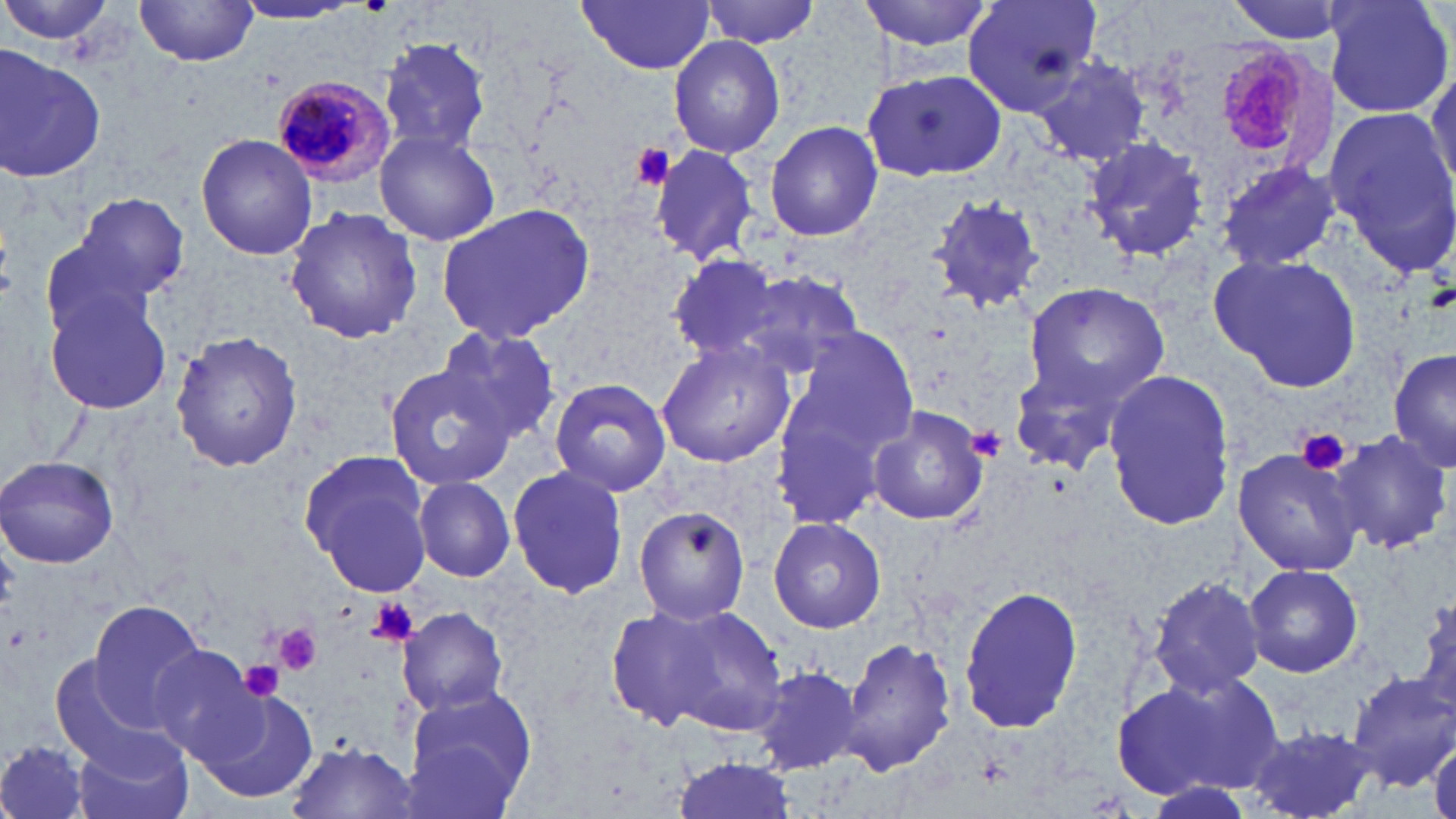

Approximate bounding boxes as named x1/y1/x2/y2 corners in pixels. Plasmodium malariae-infected red blood cell locations: (x1=1207, y1=40, x2=1314, y2=162), (x1=271, y1=75, x2=395, y2=187). Platelet locations: (x1=628, y1=144, x2=675, y2=191), (x1=970, y1=427, x2=1008, y2=459), (x1=1298, y1=428, x2=1350, y2=476), (x1=367, y1=598, x2=416, y2=644), (x1=273, y1=624, x2=325, y2=676), (x1=242, y1=661, x2=286, y2=701). Uninfected red blood cell locations: (x1=0, y1=0, x2=121, y2=51), (x1=702, y1=0, x2=822, y2=47), (x1=859, y1=0, x2=994, y2=53), (x1=962, y1=0, x2=1101, y2=117), (x1=1224, y1=0, x2=1358, y2=44), (x1=1323, y1=0, x2=1454, y2=121), (x1=133, y1=1, x2=261, y2=66), (x1=577, y1=1, x2=716, y2=74), (x1=231, y1=2, x2=361, y2=25), (x1=668, y1=33, x2=785, y2=159), (x1=378, y1=37, x2=491, y2=158), (x1=0, y1=46, x2=106, y2=184), (x1=1029, y1=56, x2=1151, y2=167), (x1=1427, y1=61, x2=1456, y2=192), (x1=863, y1=67, x2=1008, y2=183), (x1=1321, y1=104, x2=1456, y2=276), (x1=765, y1=120, x2=883, y2=241), (x1=373, y1=129, x2=501, y2=244), (x1=195, y1=133, x2=318, y2=260), (x1=1081, y1=134, x2=1209, y2=265), (x1=649, y1=143, x2=760, y2=266), (x1=1215, y1=160, x2=1340, y2=274), (x1=72, y1=192, x2=189, y2=304), (x1=926, y1=193, x2=1047, y2=315), (x1=437, y1=203, x2=595, y2=342), (x1=285, y1=209, x2=422, y2=344), (x1=37, y1=236, x2=166, y2=346), (x1=1208, y1=253, x2=1362, y2=392), (x1=667, y1=254, x2=786, y2=359), (x1=737, y1=268, x2=865, y2=378), (x1=1025, y1=279, x2=1173, y2=408), (x1=44, y1=285, x2=175, y2=416), (x1=436, y1=324, x2=562, y2=443), (x1=790, y1=324, x2=920, y2=452), (x1=170, y1=330, x2=302, y2=473), (x1=655, y1=338, x2=795, y2=468), (x1=1389, y1=349, x2=1456, y2=476), (x1=1010, y1=363, x2=1133, y2=476), (x1=384, y1=364, x2=515, y2=490), (x1=1103, y1=369, x2=1236, y2=531), (x1=549, y1=378, x2=672, y2=497), (x1=771, y1=391, x2=895, y2=530), (x1=869, y1=406, x2=989, y2=526), (x1=1327, y1=428, x2=1452, y2=556), (x1=1235, y1=446, x2=1362, y2=575), (x1=0, y1=454, x2=120, y2=568), (x1=303, y1=454, x2=434, y2=595), (x1=507, y1=464, x2=628, y2=599), (x1=414, y1=477, x2=516, y2=581), (x1=633, y1=505, x2=752, y2=626), (x1=769, y1=516, x2=885, y2=633), (x1=1244, y1=563, x2=1363, y2=677), (x1=1147, y1=574, x2=1267, y2=698), (x1=957, y1=586, x2=1085, y2=736), (x1=1411, y1=596, x2=1455, y2=718), (x1=87, y1=598, x2=209, y2=723), (x1=646, y1=603, x2=789, y2=736), (x1=399, y1=608, x2=509, y2=716), (x1=606, y1=608, x2=726, y2=728), (x1=839, y1=635, x2=956, y2=776), (x1=145, y1=644, x2=264, y2=764), (x1=754, y1=664, x2=863, y2=775), (x1=1115, y1=668, x2=1283, y2=802), (x1=1347, y1=672, x2=1456, y2=789), (x1=400, y1=685, x2=538, y2=815), (x1=198, y1=688, x2=320, y2=806), (x1=1245, y1=725, x2=1376, y2=819), (x1=73, y1=733, x2=195, y2=819), (x1=0, y1=738, x2=94, y2=819), (x1=1428, y1=738, x2=1456, y2=819), (x1=285, y1=742, x2=420, y2=819), (x1=672, y1=755, x2=801, y2=819). Slide-level diagnosis: Plasmodium malariae. Optical microscopy. Image is 1456×819 pixels. May-Grünwald-Giemsa stain. 1000x magnification. One field of a larger specimen. Thin blood film.